State the preparation type.
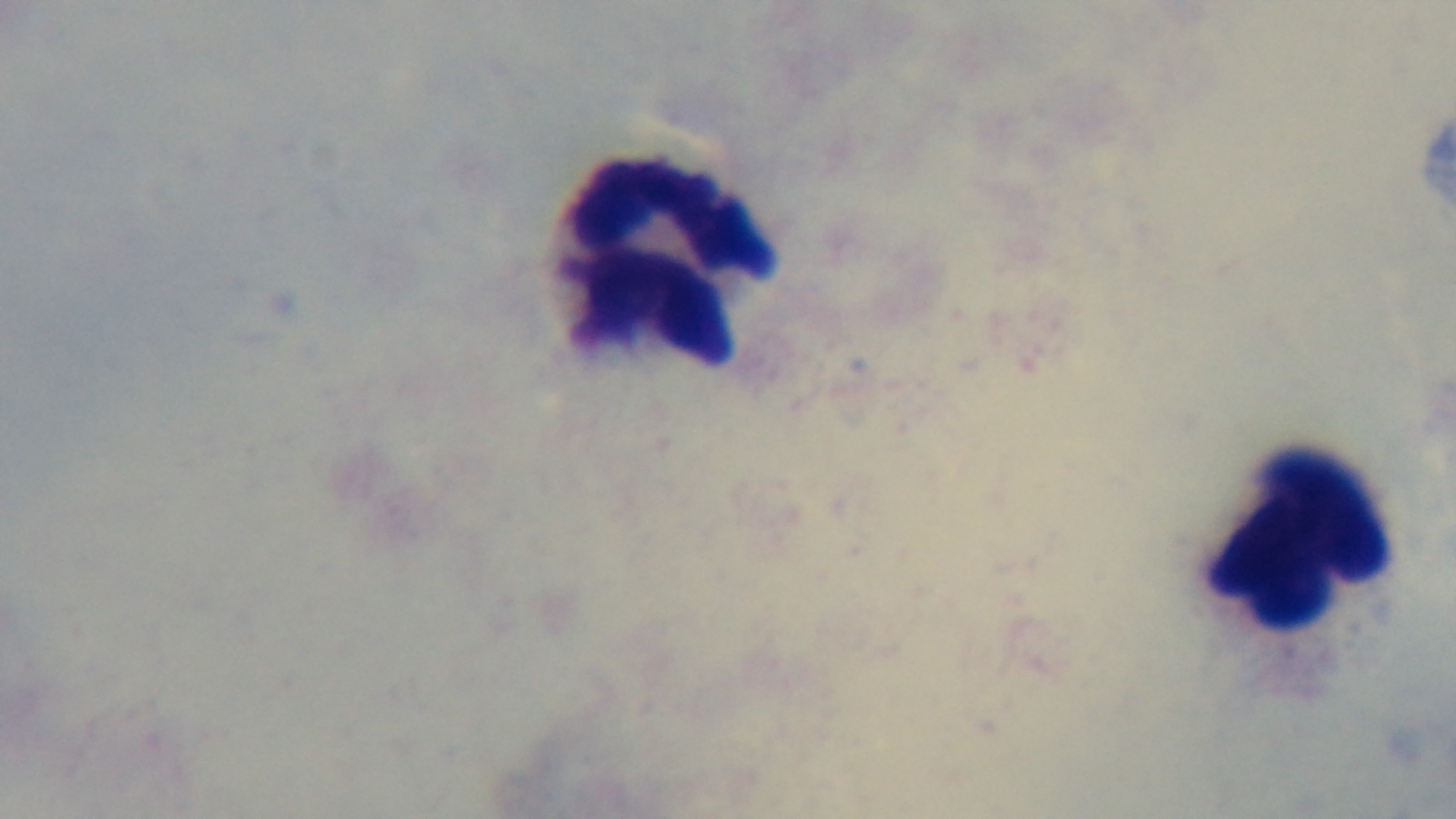

A thick smear.

Malaria status: negative. Single field of view. Captured with a mounted 4K digital camera. Light microscopy. Oil-immersion objective, 100x. Giemsa stain.